Give the position of every Plasmodium parasite visible.
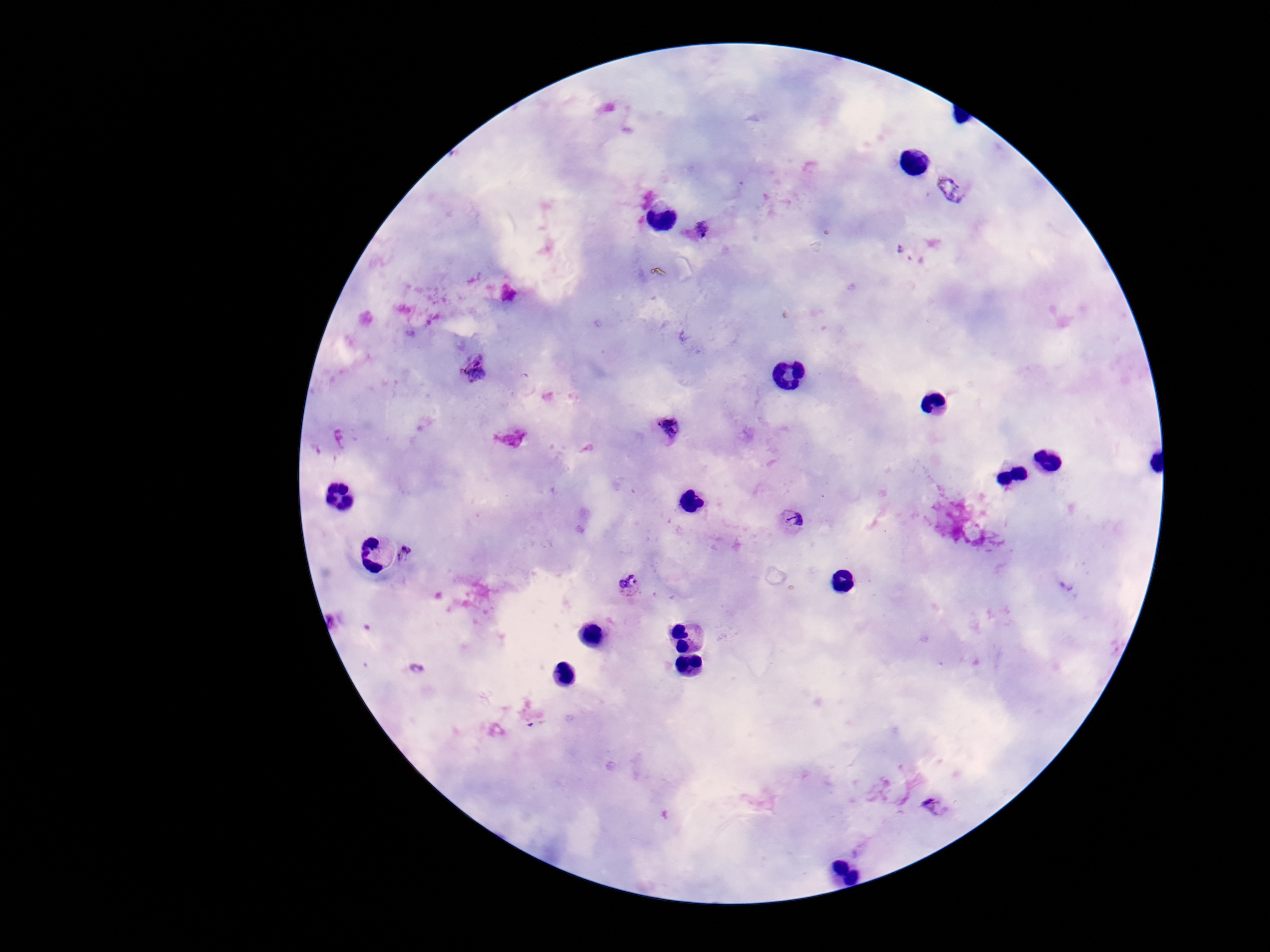
Approximate centers as (x, y) in pixels.
Plasmodium parasites: (952, 189), (702, 228), (912, 252), (473, 368), (666, 429), (792, 520), (407, 552), (628, 586), (1067, 587), (334, 620), (418, 668), (934, 805).

{
  "stain": "Giemsa",
  "capture": "smartphone camera through the microscope eyepiece",
  "patient_malaria_status": "infected",
  "field_of_view": "one from this slide",
  "preparation": "thick peripheral-blood smear",
  "magnification": "100x",
  "image_size": "1270×952 pixels"
}